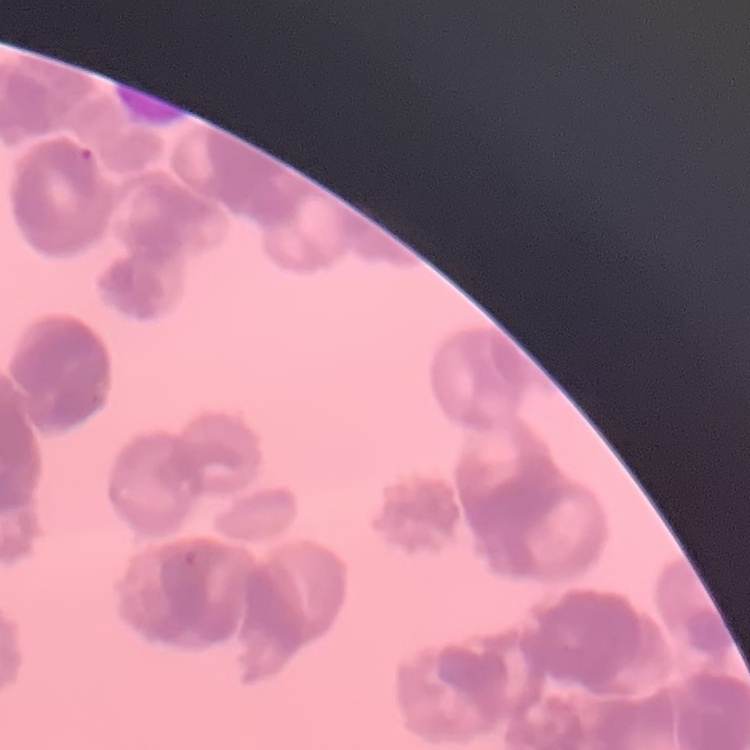

Summary:
  - Red blood cell morphology: rouleaux formation
  - Image type: square crop of a larger photomicrograph
  - Preparation: thin blood smear
  - Stain: Field's or Giemsa